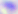

Summary:
  - Magnification: 400x
  - Identification: Toxoplasma gondii
  - Modality: micrograph